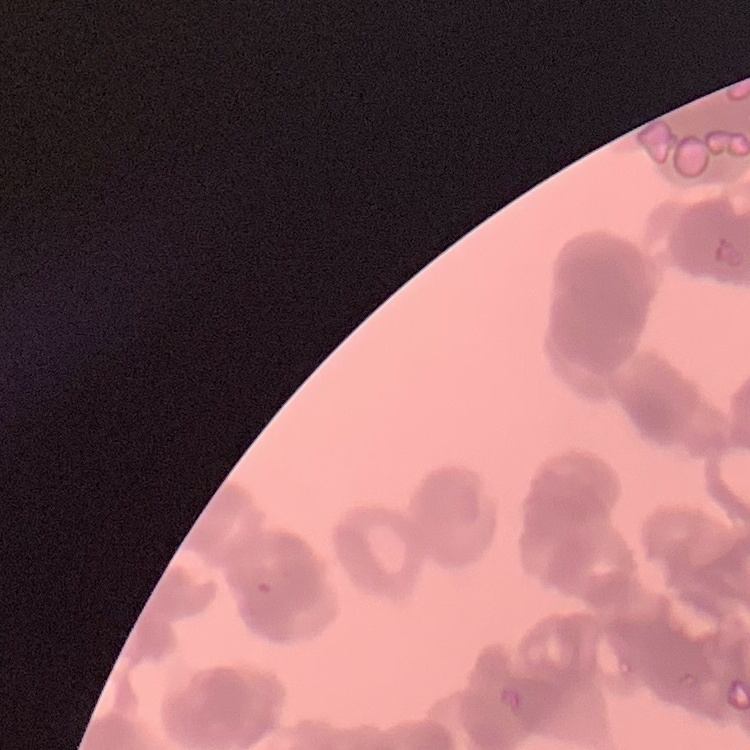
The erythrocytes exhibit rouleaux formation. Stained with either Field's or Giemsa. Thin blood smear. Square crop of a larger photomicrograph.